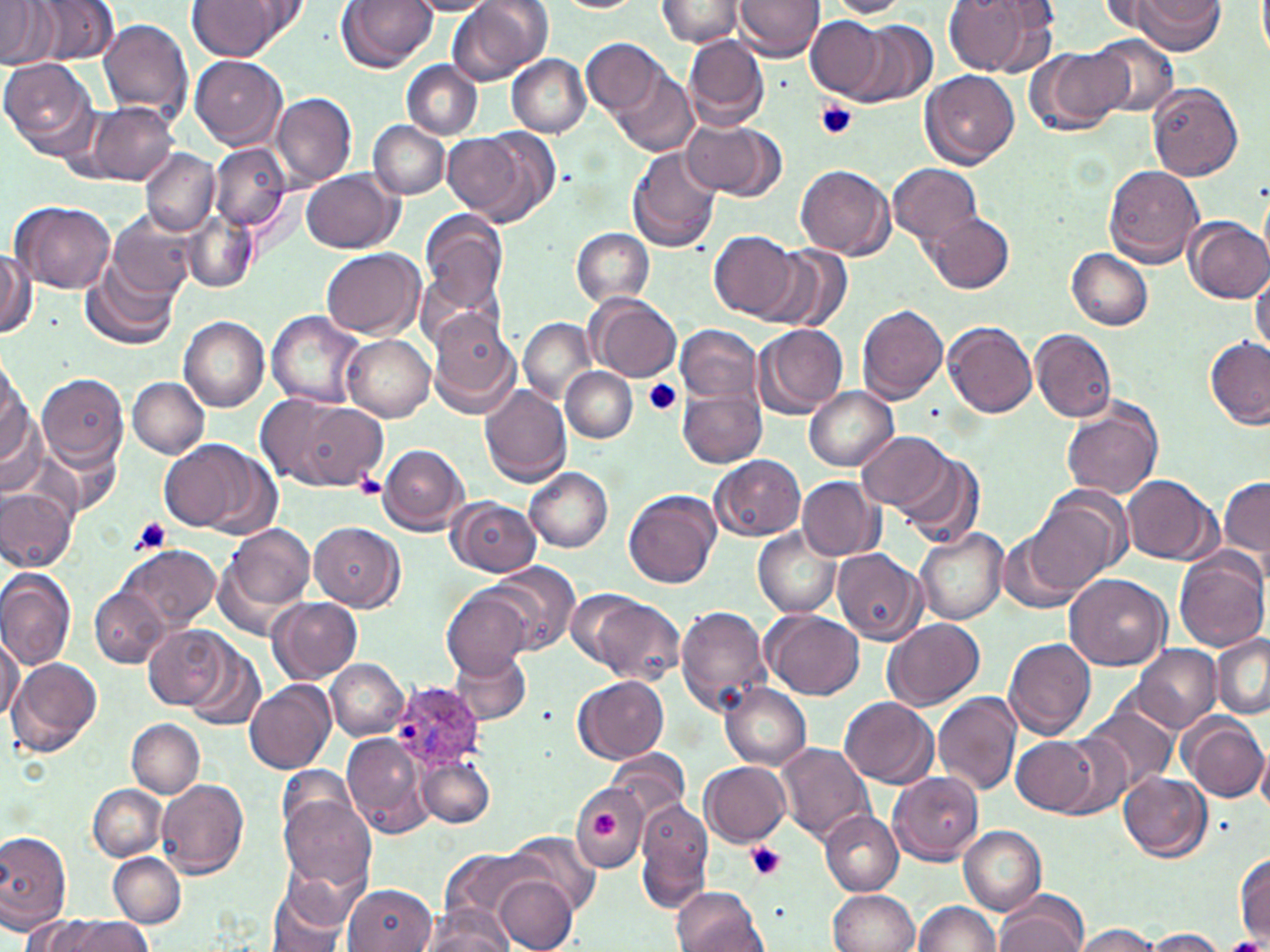
{
  "slide_level_diagnosis": "Plasmodium ovale",
  "field_of_view": "single",
  "plasmodium_ovale_infected_red_blood_cell_locations": "approximate bounding boxes as [x1, y1, x2, y2] in pixels: [390, 682, 483, 769]",
  "stain": "May-Grünwald-Giemsa",
  "image_size": "1270×952 pixels",
  "uninfected_red_blood_cell_locations": "approximate bounding boxes as [x1, y1, x2, y2] in pixels: [33, 0, 118, 65], [244, 0, 310, 40], [336, 0, 436, 72], [449, 0, 550, 85], [735, 0, 823, 60], [825, 0, 912, 19], [943, 0, 1053, 78], [187, 1, 285, 59], [406, 1, 496, 16], [550, 1, 644, 12], [657, 1, 745, 47], [1097, 1, 1184, 38], [1134, 1, 1227, 53], [0, 3, 54, 68], [806, 16, 891, 101], [99, 19, 194, 122], [853, 22, 937, 105], [1088, 32, 1178, 116], [685, 35, 769, 131], [583, 37, 666, 118], [1027, 46, 1129, 137], [506, 54, 591, 136], [189, 55, 287, 148], [0, 57, 100, 159], [400, 60, 483, 138], [921, 71, 1020, 169], [616, 74, 696, 155], [1146, 82, 1245, 180], [271, 91, 358, 188], [90, 102, 179, 184], [369, 121, 450, 199], [683, 122, 785, 201], [339, 125, 434, 225], [468, 126, 561, 226], [444, 132, 527, 218], [209, 143, 293, 235], [628, 146, 723, 254], [141, 149, 218, 237], [887, 161, 983, 248], [796, 164, 896, 260], [1103, 165, 1205, 268], [302, 170, 401, 253], [11, 201, 115, 295], [419, 210, 507, 317], [110, 211, 200, 298], [925, 212, 1014, 294], [183, 213, 258, 292], [1184, 216, 1269, 303], [571, 227, 656, 307], [709, 230, 800, 321], [765, 245, 851, 334], [322, 248, 424, 338], [1068, 249, 1153, 329], [0, 250, 35, 340], [82, 260, 180, 350], [1249, 267, 1269, 358], [589, 295, 681, 382], [856, 303, 947, 403], [266, 310, 366, 410], [427, 312, 520, 418], [180, 316, 271, 411], [519, 317, 595, 404], [943, 321, 1039, 419], [676, 324, 762, 409], [754, 324, 848, 418], [1030, 329, 1117, 422], [342, 332, 435, 421], [1204, 337, 1269, 429], [0, 357, 31, 474], [561, 366, 637, 443], [37, 372, 129, 471], [128, 377, 210, 458], [479, 385, 574, 486], [804, 386, 898, 469], [678, 387, 765, 467], [257, 394, 387, 492], [1061, 402, 1164, 498], [0, 408, 48, 504], [856, 431, 955, 515], [39, 435, 126, 516], [160, 439, 265, 534], [377, 444, 470, 534], [894, 451, 983, 548], [712, 455, 806, 541], [526, 468, 613, 551], [1122, 473, 1219, 563], [797, 475, 884, 560], [1218, 475, 1270, 564], [449, 481, 614, 563], [0, 485, 76, 571], [624, 490, 721, 589], [446, 496, 541, 576], [1026, 496, 1121, 595], [308, 521, 404, 611], [224, 525, 316, 614], [914, 527, 1009, 626], [754, 528, 841, 618], [998, 534, 1084, 614], [119, 543, 220, 632], [832, 548, 926, 644], [1174, 549, 1269, 652], [486, 562, 581, 656], [0, 573, 75, 669], [1065, 574, 1173, 672], [91, 586, 170, 668], [441, 588, 531, 677], [563, 589, 648, 672], [1026, 592, 1130, 707], [584, 595, 684, 686], [269, 596, 363, 685], [674, 605, 772, 716], [766, 611, 866, 701], [884, 619, 985, 710], [144, 623, 230, 710], [0, 632, 22, 724], [1210, 632, 1270, 719], [1002, 638, 1098, 741], [181, 640, 265, 732], [1132, 644, 1222, 733], [448, 650, 530, 726], [7, 657, 103, 757], [326, 659, 408, 740], [574, 676, 669, 763], [245, 679, 336, 773], [719, 684, 812, 770], [932, 692, 1022, 796], [839, 696, 938, 787], [1079, 701, 1178, 798], [1180, 712, 1270, 803], [127, 718, 203, 798], [344, 733, 435, 842], [1012, 734, 1100, 814], [1044, 734, 1137, 819], [775, 742, 874, 845], [1258, 743, 1270, 819], [608, 751, 690, 825], [416, 754, 495, 828], [700, 760, 791, 847], [277, 764, 362, 836], [887, 771, 983, 864], [1120, 772, 1211, 861], [156, 780, 249, 879], [571, 782, 648, 870], [88, 783, 166, 861], [279, 793, 374, 891], [634, 799, 713, 909], [820, 810, 905, 894], [958, 824, 1046, 914], [508, 831, 600, 915], [0, 832, 72, 930], [441, 847, 544, 930], [109, 852, 185, 928], [275, 852, 372, 934], [1234, 853, 1269, 943], [493, 875, 578, 951], [342, 885, 437, 952], [265, 887, 349, 952], [671, 887, 765, 952], [828, 889, 919, 952], [995, 893, 1089, 952], [912, 900, 1003, 952], [423, 905, 514, 951], [23, 913, 96, 951], [61, 917, 154, 952], [1072, 924, 1162, 951], [1146, 928, 1227, 951]",
  "preparation": "thin blood film",
  "platelet_locations": "approximate bounding boxes as [x1, y1, x2, y2] in pixels: [817, 101, 857, 141], [643, 379, 682, 416], [352, 471, 387, 498], [128, 517, 172, 555], [592, 813, 619, 839], [746, 841, 786, 882]",
  "modality": "optical microscopy",
  "magnification": "1000x"
}